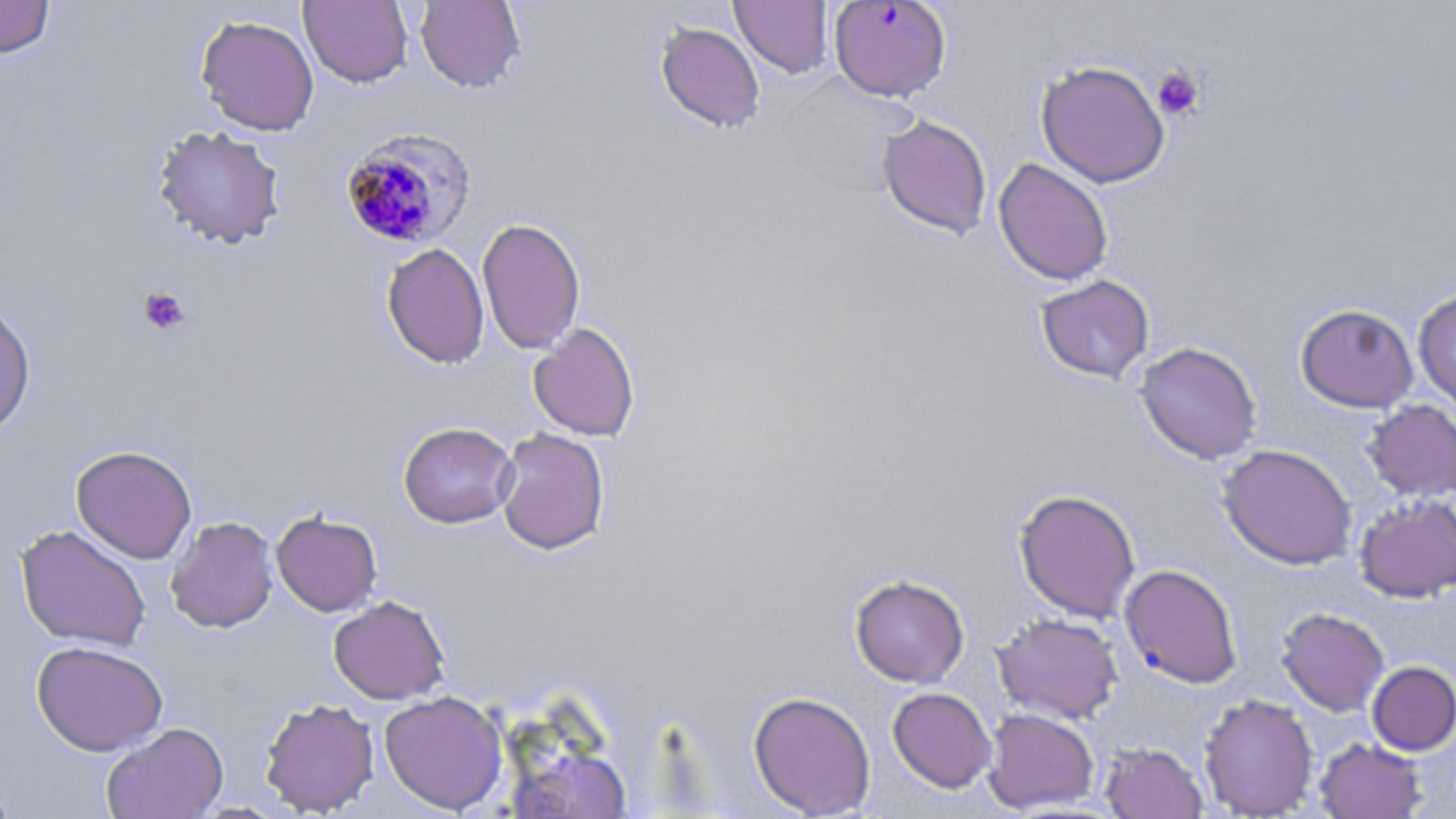
Summary:
  - Coordinate format: approximate bounding boxes as [x1, y1, x2, y2] in pixels
  - Plasmodium falciparum-infected red blood cell locations: [828, 1, 952, 102], [338, 127, 477, 249]
  - Uninfected red blood cell locations: [0, 0, 55, 59], [299, 0, 413, 88], [415, 0, 526, 93], [730, 0, 834, 79], [195, 14, 319, 136], [655, 22, 765, 134], [1035, 59, 1170, 188], [770, 73, 918, 199], [877, 114, 993, 239], [152, 124, 287, 250], [992, 157, 1113, 286], [477, 217, 586, 355], [382, 243, 490, 369], [1036, 274, 1154, 383], [1412, 288, 1456, 413], [0, 299, 36, 438], [1295, 303, 1419, 412], [528, 322, 640, 441], [1135, 341, 1262, 464], [1362, 400, 1456, 501], [398, 422, 518, 528], [494, 427, 610, 555], [1218, 443, 1358, 570], [70, 445, 197, 564], [1013, 488, 1141, 622], [1354, 493, 1456, 602], [271, 510, 383, 616], [165, 516, 279, 633], [15, 523, 151, 652], [1119, 564, 1242, 688], [849, 574, 970, 687], [328, 595, 450, 705], [1276, 607, 1389, 716], [992, 612, 1124, 724], [31, 640, 168, 756], [1367, 661, 1456, 755], [887, 687, 997, 793], [379, 691, 508, 814], [748, 691, 876, 817], [1199, 693, 1319, 818], [259, 697, 380, 816], [981, 707, 1100, 813], [102, 722, 228, 819], [1315, 737, 1426, 818], [1101, 742, 1208, 818], [0, 778, 19, 817]
  - Platelet locations: [1152, 67, 1204, 120], [137, 286, 191, 336]
  - Slide-level diagnosis: Plasmodium falciparum
  - Stain: May-Grünwald-Giemsa
  - Field of view: one of a larger specimen
  - Preparation: thin blood smear
  - Modality: light microscopy
  - Magnification: 1000x
  - Image size: 1456×819 pixels